State which parasite is depicted.
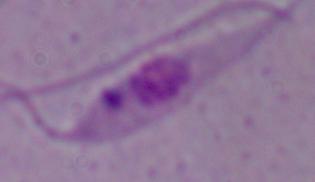
This is Leishmania.

Summary:
  - Modality: photomicrograph
  - Magnification: 1000x